Describe the morphology of the erythrocytes.
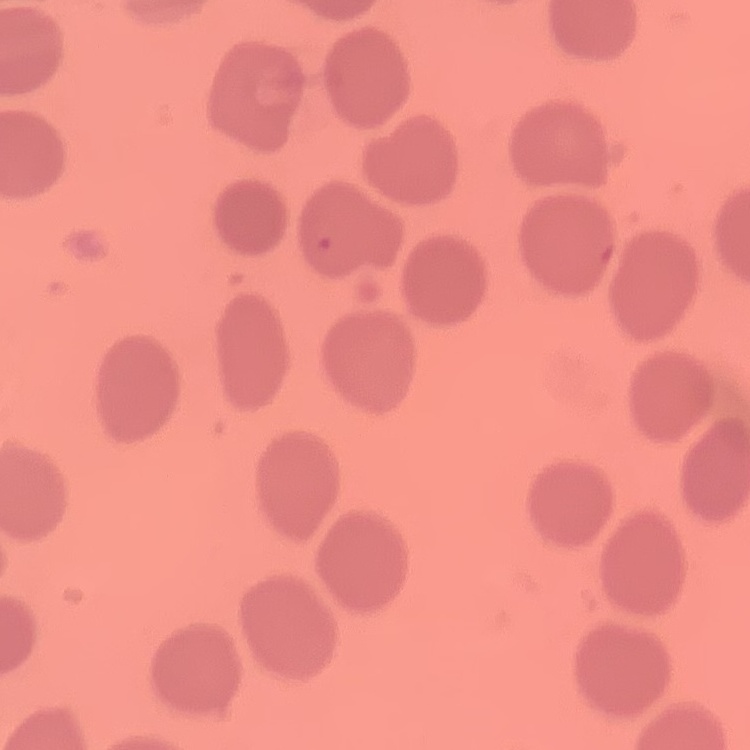

No rouleaux formation.

image type = square crop of a larger photomicrograph
stain = Field's or Giemsa
preparation = thin peripheral smear